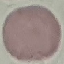
Malaria status: uninfected. Cell patch, automatically extracted from a larger field of view and resized to 64 × 64 pixels. Thin smear of blood. Giemsa stain. Acquired by smartphone through the microscope eyepiece.